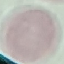
Result: no malaria parasites detected. Giemsa-stained preparation. Thin smear of blood. Cell patch, automatically extracted from a larger field of view and resized to 64 × 64 pixels. Photographed with a smartphone camera at the microscope eyepiece.